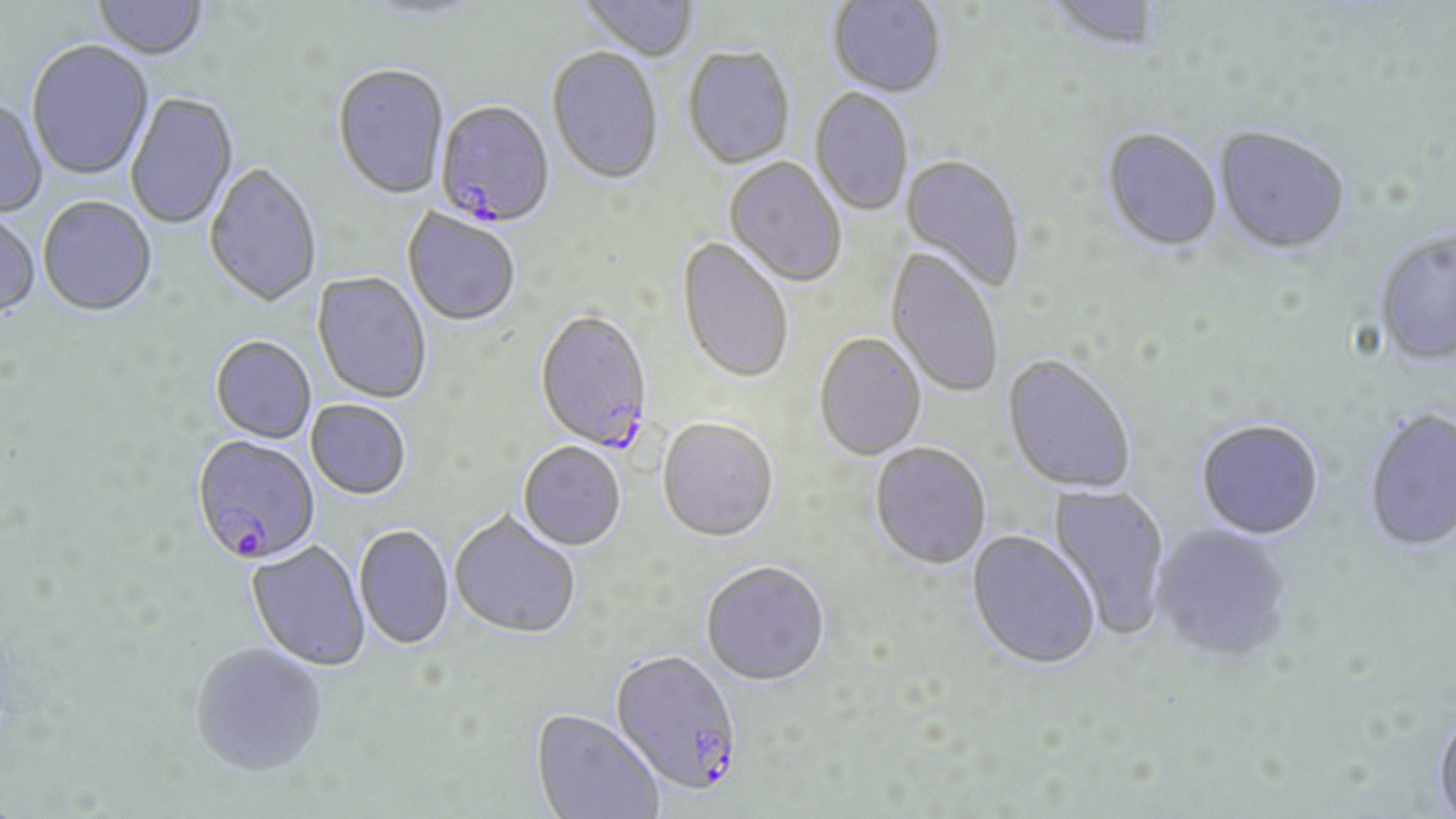

Approximate bounding boxes as (x1,y1)-(x2,y2) corner pairs in pixels. Uninfected red blood cell locations: (92,0)-(208,62), (361,0)-(484,23), (579,0)-(699,63), (1045,0)-(1164,54), (826,1)-(946,99), (26,42)-(154,182), (682,47)-(796,171), (547,49)-(664,187), (332,65)-(449,202), (809,89)-(913,217), (125,93)-(239,230), (0,99)-(47,218), (1214,126)-(1351,257), (1101,129)-(1223,255), (899,155)-(1025,293), (723,157)-(847,288), (204,164)-(321,310), (38,198)-(157,318), (402,209)-(520,328), (0,212)-(41,321), (1373,230)-(1456,367), (676,238)-(794,386), (884,247)-(1003,399), (312,272)-(431,405), (813,335)-(926,462), (210,337)-(316,444), (1002,354)-(1137,496), (306,401)-(410,501), (1363,409)-(1456,552), (657,420)-(778,545), (1195,421)-(1324,541), (518,443)-(626,552), (869,444)-(991,571), (1047,483)-(1171,640), (449,513)-(580,641), (1151,525)-(1293,664), (353,526)-(454,651), (966,531)-(1101,672), (246,541)-(370,672), (700,563)-(829,690), (189,643)-(328,776), (1433,703)-(1456,819), (530,711)-(664,819). Plasmodium falciparum-infected red blood cell locations: (435,103)-(554,229), (533,312)-(653,453), (191,436)-(320,568), (610,651)-(743,798). Slide-level diagnosis: Plasmodium falciparum. Optical microscopy. Thin blood film. Image is 1456×819 pixels. One field of a larger specimen. May-Grünwald-Giemsa stain. 1000x magnification.